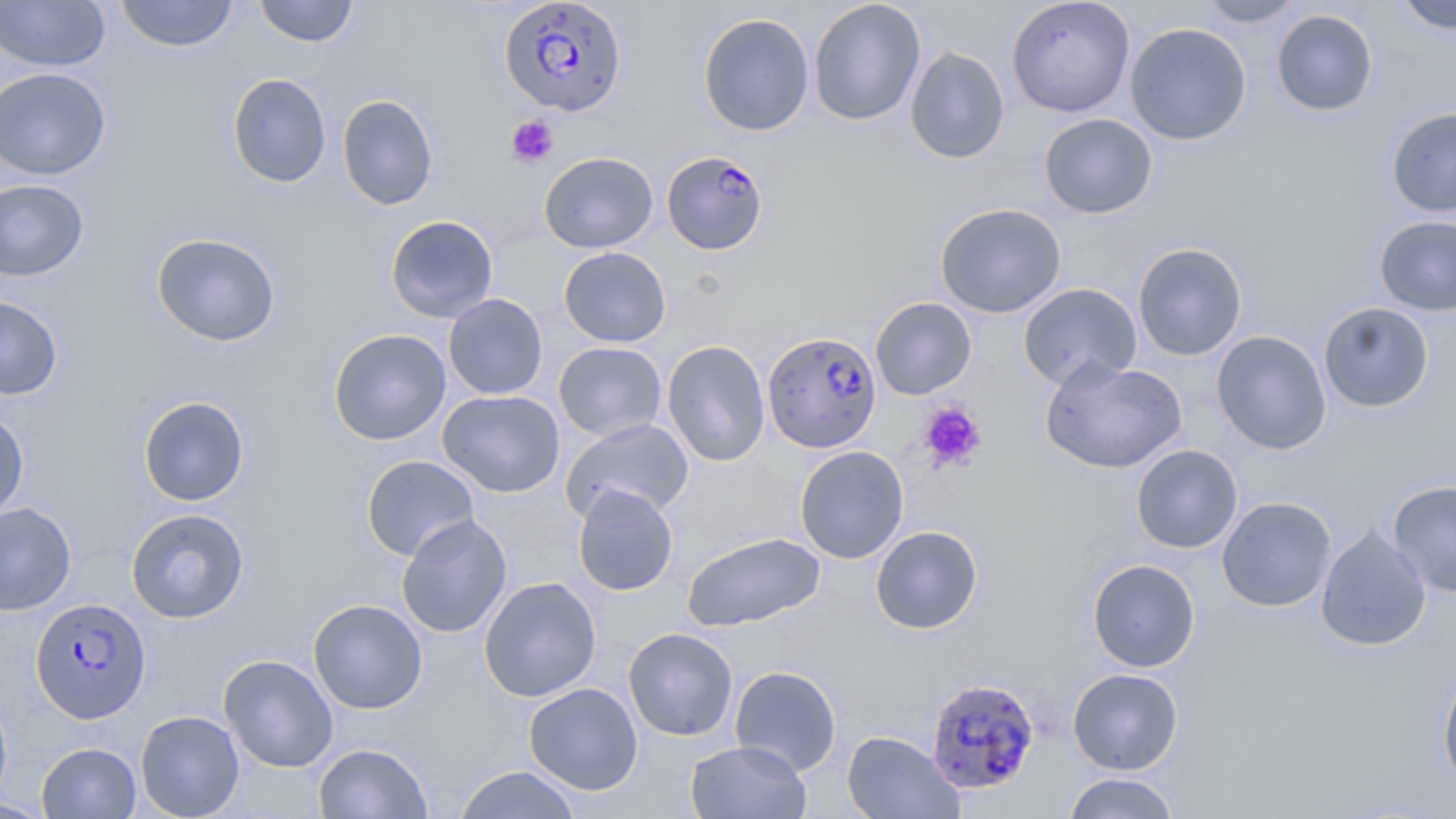

Summary:
  - Coordinate format: approximate bounding boxes as named x1/y1/x2/y2 corners in pixels
  - Uninfected red blood cell locations: (x1=115, y1=0, x2=239, y2=52), (x1=254, y1=0, x2=359, y2=47), (x1=808, y1=0, x2=926, y2=126), (x1=1006, y1=0, x2=1135, y2=117), (x1=1198, y1=0, x2=1308, y2=28), (x1=1393, y1=0, x2=1456, y2=34), (x1=0, y1=1, x2=111, y2=72), (x1=1271, y1=8, x2=1379, y2=117), (x1=698, y1=13, x2=815, y2=136), (x1=1125, y1=22, x2=1252, y2=145), (x1=904, y1=45, x2=1010, y2=165), (x1=0, y1=67, x2=112, y2=180), (x1=227, y1=73, x2=332, y2=189), (x1=337, y1=94, x2=439, y2=210), (x1=1385, y1=107, x2=1456, y2=217), (x1=1039, y1=113, x2=1158, y2=218), (x1=539, y1=151, x2=658, y2=253), (x1=0, y1=178, x2=89, y2=282), (x1=934, y1=202, x2=1067, y2=318), (x1=385, y1=215, x2=498, y2=322), (x1=1374, y1=216, x2=1456, y2=316), (x1=151, y1=232, x2=281, y2=347), (x1=1132, y1=242, x2=1248, y2=360), (x1=558, y1=246, x2=671, y2=347), (x1=1017, y1=283, x2=1142, y2=390), (x1=443, y1=294, x2=548, y2=399), (x1=0, y1=295, x2=64, y2=401), (x1=870, y1=297, x2=977, y2=400), (x1=1318, y1=302, x2=1434, y2=413), (x1=328, y1=328, x2=451, y2=445), (x1=1211, y1=330, x2=1332, y2=454), (x1=661, y1=339, x2=771, y2=467), (x1=554, y1=341, x2=667, y2=442), (x1=1040, y1=357, x2=1187, y2=474), (x1=437, y1=389, x2=565, y2=497), (x1=137, y1=396, x2=250, y2=506), (x1=0, y1=410, x2=30, y2=522), (x1=561, y1=418, x2=694, y2=523), (x1=1130, y1=444, x2=1243, y2=553), (x1=794, y1=445, x2=909, y2=564), (x1=360, y1=455, x2=480, y2=562), (x1=1387, y1=479, x2=1456, y2=598), (x1=572, y1=483, x2=678, y2=596), (x1=1217, y1=496, x2=1337, y2=612), (x1=0, y1=502, x2=77, y2=616), (x1=125, y1=508, x2=250, y2=623), (x1=396, y1=514, x2=513, y2=638), (x1=1315, y1=525, x2=1432, y2=652), (x1=870, y1=526, x2=983, y2=634), (x1=681, y1=531, x2=825, y2=631), (x1=1087, y1=558, x2=1201, y2=672), (x1=478, y1=577, x2=602, y2=701), (x1=308, y1=598, x2=429, y2=714), (x1=623, y1=627, x2=738, y2=741), (x1=218, y1=654, x2=339, y2=772), (x1=1437, y1=663, x2=1456, y2=791), (x1=729, y1=664, x2=842, y2=776), (x1=1067, y1=668, x2=1183, y2=775), (x1=524, y1=682, x2=643, y2=794), (x1=0, y1=688, x2=13, y2=809), (x1=135, y1=710, x2=245, y2=819), (x1=842, y1=731, x2=965, y2=819), (x1=685, y1=740, x2=812, y2=818), (x1=36, y1=742, x2=141, y2=818), (x1=313, y1=742, x2=432, y2=818), (x1=452, y1=764, x2=583, y2=818), (x1=1062, y1=772, x2=1182, y2=819), (x1=0, y1=798, x2=55, y2=818)
  - Platelet locations: (x1=506, y1=115, x2=559, y2=167), (x1=918, y1=401, x2=987, y2=472)
  - Plasmodium falciparum-infected red blood cell locations: (x1=499, y1=0, x2=628, y2=117), (x1=663, y1=154, x2=769, y2=258), (x1=763, y1=331, x2=882, y2=453), (x1=30, y1=597, x2=151, y2=723), (x1=925, y1=676, x2=1041, y2=795)
  - Slide-level diagnosis: Plasmodium falciparum
  - Magnification: 1000x
  - Image size: 1456×819 pixels
  - Stain: May-Grünwald-Giemsa
  - Field of view: one of a larger specimen
  - Modality: optical microscopy
  - Preparation: thin blood smear